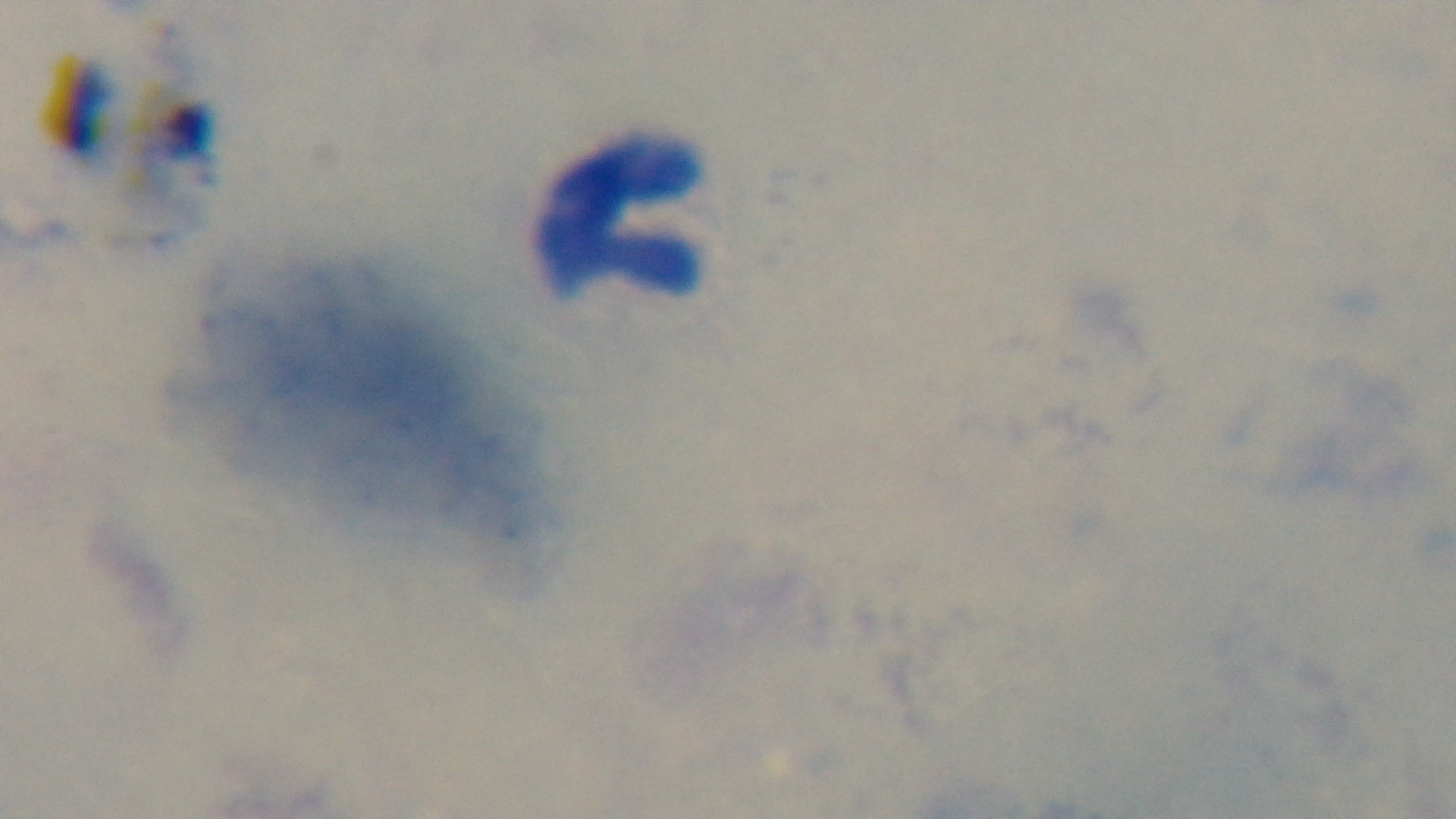

capture = mounted 4K digital camera
modality = light microscopy
preparation = thick blood film
stain = Giemsa
malaria status = uninfected
field of view = single
objective = 100x oil immersion